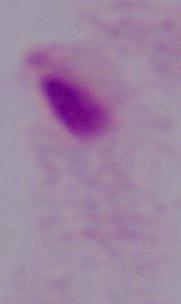

Photomicrograph. Captured at 1000x magnification. A trichomonad is seen.